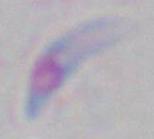
Summary:
  - Modality: photomicrograph
  - Magnification: 1000x
  - Identification: Toxoplasma gondii